State which parasite is depicted.
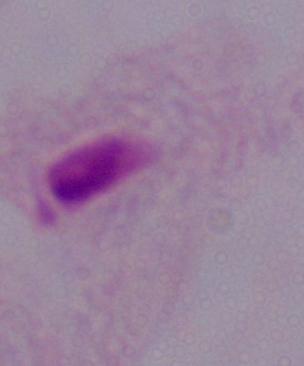

This is a trichomonad.

Summary:
  - Magnification: 1000x
  - Modality: micrograph